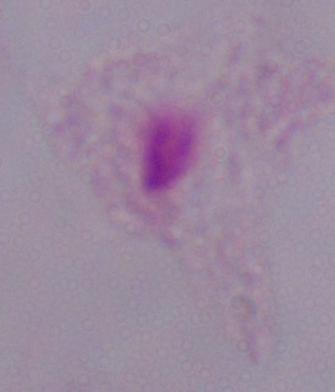

Summary:
  - Identification: trichomonad
  - Magnification: 1000x
  - Modality: photomicrograph